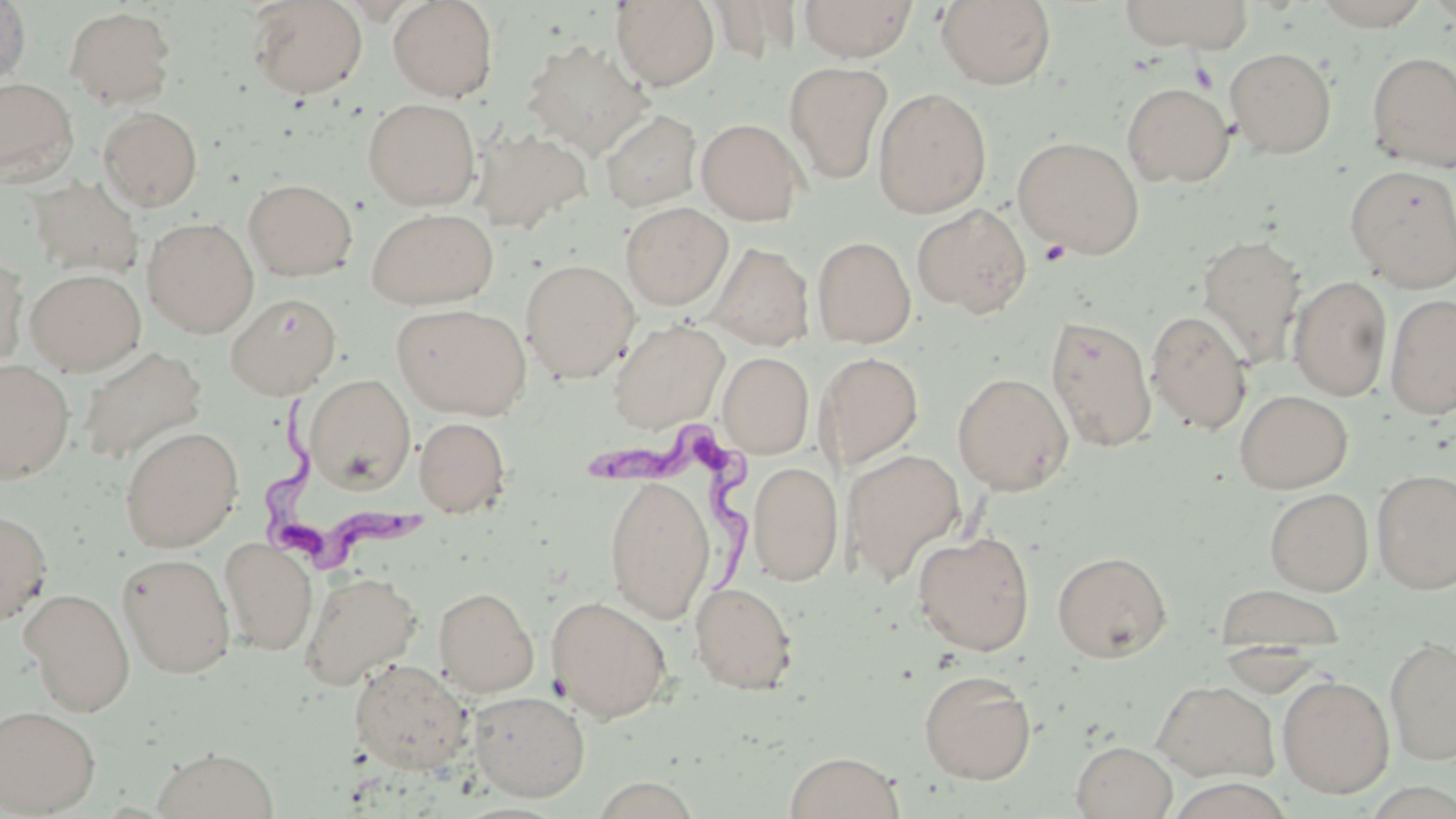
Approximate bounding boxes as (x1, y1, x2, y2) in pixels. Trypanosoma brucei locations: (257, 397, 421, 573), (586, 424, 753, 585). Uninfected red blood cell locations: (247, 0, 367, 99), (387, 0, 498, 101), (611, 0, 720, 90), (799, 0, 918, 62), (935, 0, 1057, 90), (1118, 0, 1253, 52), (1309, 0, 1433, 30), (1421, 0, 1456, 25), (0, 1, 32, 90), (705, 2, 800, 63), (65, 6, 176, 109), (521, 39, 653, 159), (1225, 47, 1337, 158), (1366, 51, 1456, 172), (785, 61, 894, 185), (0, 77, 78, 184), (1121, 82, 1234, 187), (873, 87, 992, 218), (363, 98, 480, 210), (98, 106, 203, 211), (600, 109, 702, 211), (696, 118, 806, 225), (473, 127, 592, 234), (1012, 136, 1145, 258), (1346, 164, 1456, 291), (27, 177, 145, 278), (243, 178, 358, 281), (620, 202, 733, 310), (912, 204, 1032, 317), (366, 207, 499, 309), (142, 216, 259, 338), (1196, 233, 1307, 369), (812, 236, 916, 348), (708, 243, 814, 350), (0, 247, 28, 371), (520, 258, 640, 383), (25, 268, 146, 375), (1289, 276, 1392, 401), (225, 293, 342, 400), (1385, 293, 1456, 419), (391, 303, 531, 419), (1147, 310, 1252, 434), (1045, 314, 1157, 452), (607, 318, 729, 433), (77, 345, 207, 466), (718, 352, 814, 458), (814, 352, 924, 470), (0, 359, 75, 484), (952, 372, 1074, 495), (304, 374, 415, 492), (1234, 389, 1352, 493), (414, 417, 510, 517), (119, 426, 243, 553), (840, 448, 966, 585), (748, 461, 843, 585), (1372, 468, 1456, 593), (604, 476, 716, 623), (1264, 487, 1373, 595), (0, 510, 52, 626), (912, 530, 1036, 656), (219, 537, 318, 655), (1052, 550, 1172, 662), (117, 552, 236, 678), (299, 571, 421, 690), (689, 581, 799, 694), (1214, 584, 1346, 660), (433, 587, 539, 697), (21, 588, 135, 716), (547, 595, 672, 722), (1385, 636, 1456, 765), (349, 658, 473, 775), (918, 669, 1037, 784), (1278, 674, 1394, 798), (1152, 680, 1280, 783), (468, 690, 590, 801), (0, 704, 101, 816), (1072, 741, 1177, 819), (151, 747, 279, 819), (783, 751, 905, 819), (591, 775, 704, 818). Platelet locations: (1188, 62, 1220, 93), (1039, 239, 1072, 266). Slide-level diagnosis: Trypanosoma brucei. One field of a larger specimen. Image is 1456×819 pixels. 1000x magnification. Light microscopy. May-Grünwald-Giemsa stain. Thin blood film.